Describe the morphology of the erythrocytes.
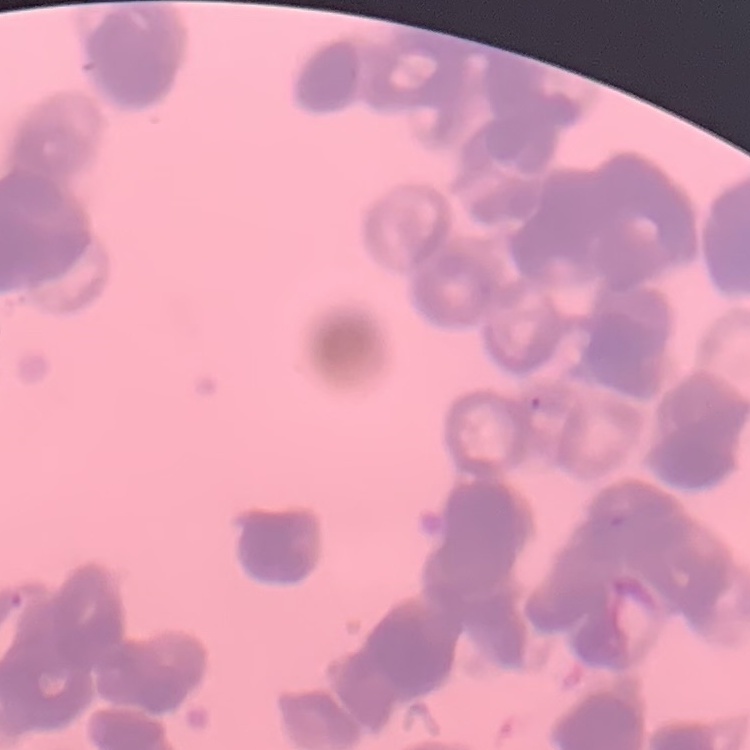

They show rouleaux formation.

Summary:
  - Image type: one tile cut from a larger photomicrograph
  - Preparation: thin peripheral smear
  - Stain: Field's or Giemsa